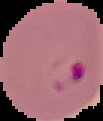 From a thin blood film. Cell region segmented out of the field of view; the surrounding area is masked to black. Image is 103×121 pixels. Result: malaria parasites identified.